Report the malaria status.
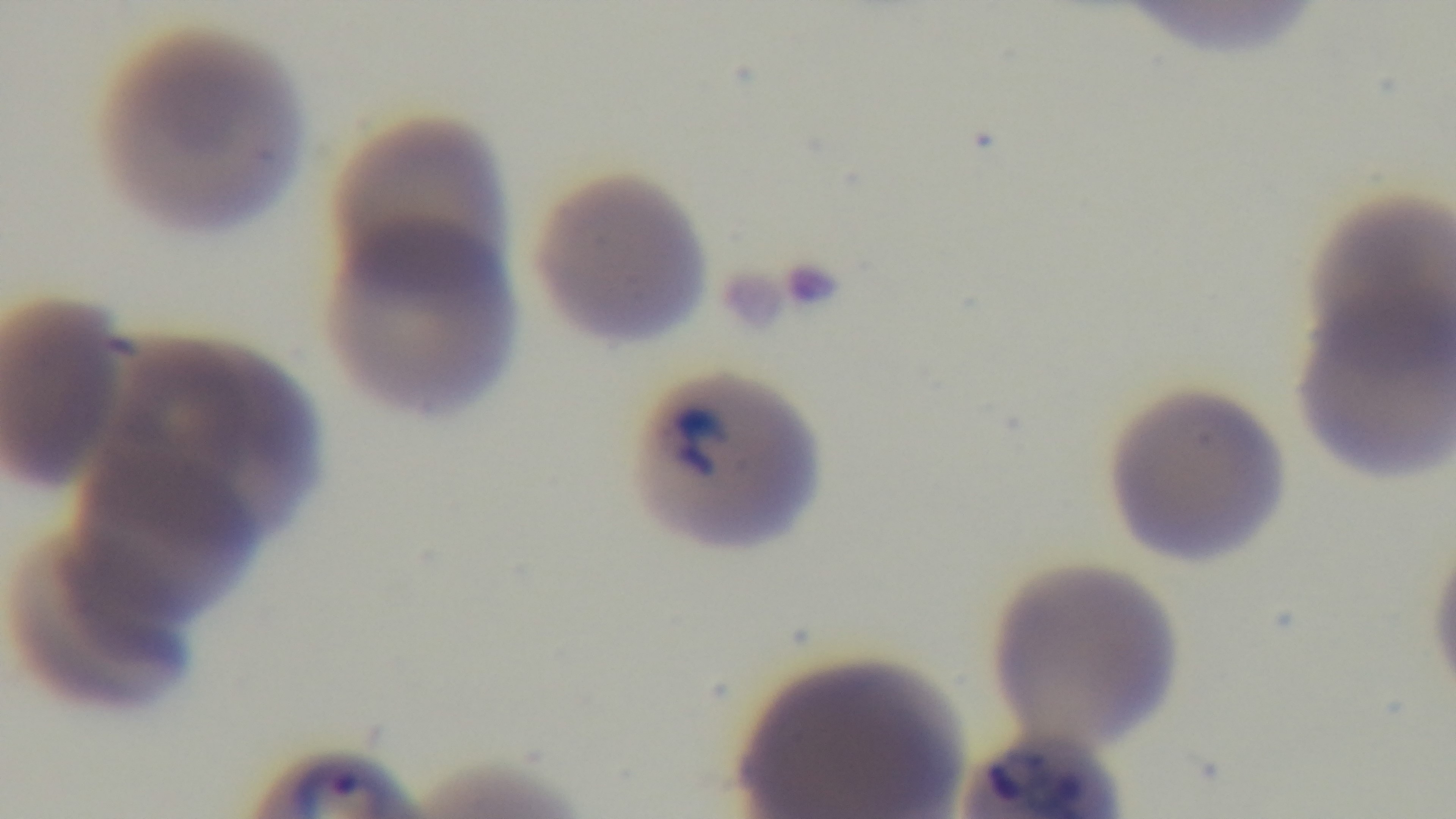

Infected.

Photomicrograph. Giemsa stain. One field from the slide. Preparation: thin. Oil-immersion objective, 100x. Captured with a mounted 4K digital camera.